Outline each Plasmodium ovale-infected red blood cell.
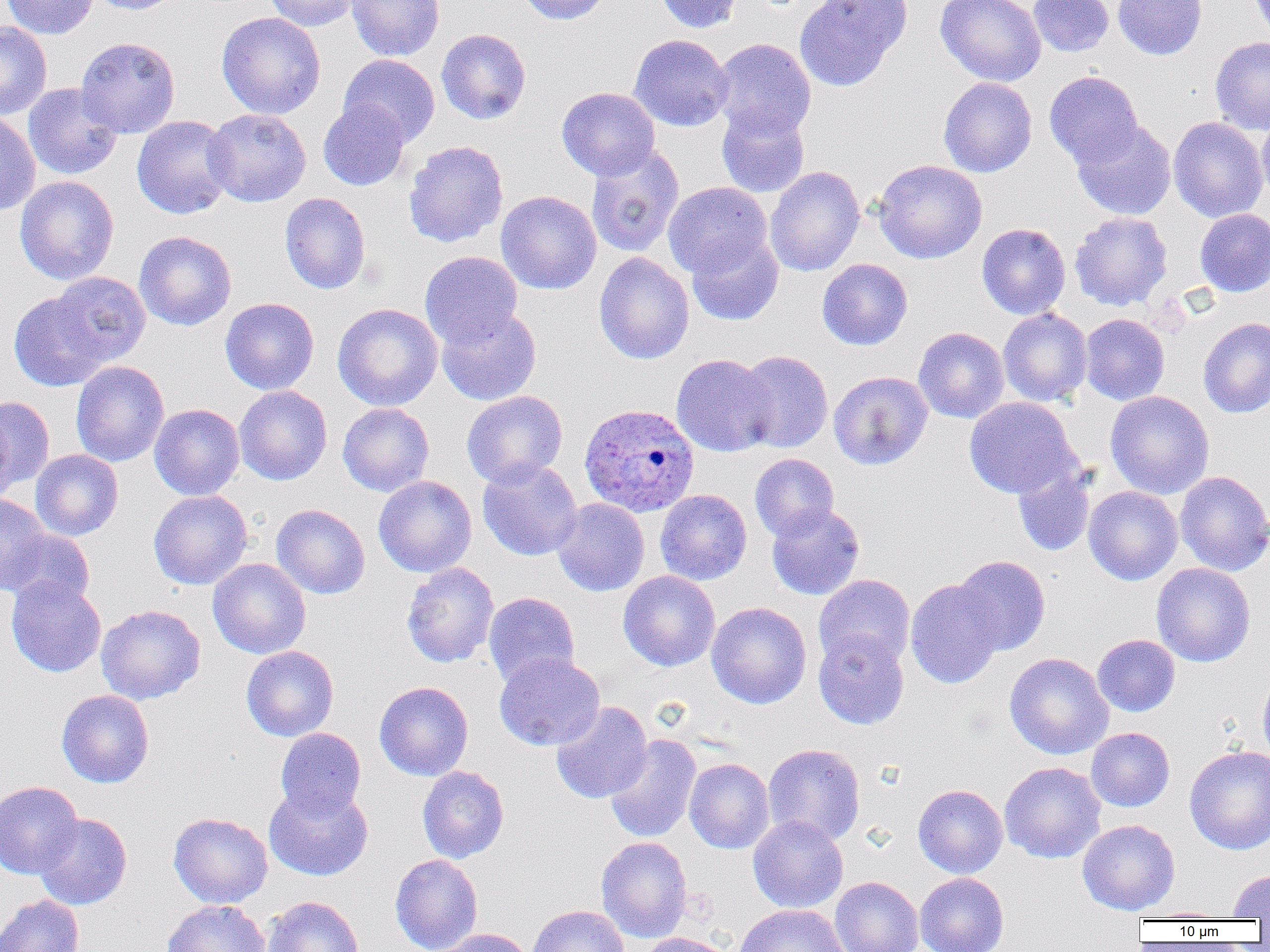
Approximate bounding boxes as (x1, y1, x2, y2) in pixels.
Plasmodium ovale-infected red blood cells: (579, 403, 699, 517).

Uninfected red blood cell locations: (2, 0, 98, 39), (86, 0, 184, 15), (262, 0, 360, 32), (346, 0, 445, 62), (517, 0, 611, 25), (653, 0, 743, 34), (794, 0, 912, 91), (934, 0, 1047, 87), (1028, 0, 1114, 57), (1113, 0, 1207, 60), (1249, 0, 1270, 39), (216, 12, 326, 119), (0, 21, 52, 119), (436, 28, 531, 125), (629, 34, 733, 132), (75, 36, 181, 138), (1210, 37, 1270, 134), (711, 38, 816, 140), (338, 54, 440, 147), (1044, 71, 1143, 168), (938, 77, 1037, 177), (23, 83, 123, 180), (556, 87, 660, 181), (318, 100, 410, 191), (716, 105, 810, 198), (203, 109, 311, 206), (0, 111, 40, 215), (1256, 111, 1270, 208), (131, 115, 236, 219), (1168, 117, 1268, 222), (1071, 120, 1177, 220), (403, 140, 508, 248), (585, 143, 684, 258), (873, 159, 987, 264), (765, 166, 865, 277), (14, 175, 119, 285), (663, 182, 772, 278), (496, 190, 601, 294), (280, 192, 371, 294), (1195, 208, 1270, 297), (1070, 211, 1172, 311), (977, 223, 1071, 320), (134, 231, 236, 331), (687, 233, 784, 326), (420, 250, 523, 347), (593, 252, 694, 364), (817, 259, 913, 350), (50, 271, 151, 366), (9, 291, 109, 391), (220, 297, 319, 395), (332, 303, 443, 411), (436, 305, 541, 405), (998, 308, 1093, 406), (1080, 313, 1170, 405), (1198, 318, 1270, 418), (913, 327, 1010, 424), (736, 350, 833, 453), (671, 354, 777, 457), (70, 360, 169, 467), (828, 370, 933, 470), (234, 385, 332, 485), (462, 390, 568, 488), (1105, 390, 1214, 499), (0, 395, 54, 495), (964, 397, 1079, 498), (0, 400, 19, 505), (337, 403, 435, 496), (149, 404, 244, 500), (30, 449, 123, 541), (749, 453, 839, 541), (477, 458, 583, 561), (1013, 464, 1096, 557), (1174, 470, 1270, 576), (373, 475, 477, 577), (1084, 486, 1183, 585), (148, 489, 252, 590), (655, 489, 752, 585), (0, 494, 51, 595), (552, 498, 650, 596), (766, 503, 865, 600), (271, 504, 370, 599), (2, 529, 94, 609), (951, 555, 1050, 656), (208, 558, 311, 659), (401, 561, 499, 668), (1151, 563, 1256, 667), (618, 571, 720, 671), (813, 574, 915, 670), (6, 576, 106, 677), (905, 578, 1006, 689), (483, 592, 580, 688), (706, 602, 811, 709), (96, 604, 205, 705), (813, 630, 909, 729), (1092, 634, 1180, 717), (241, 646, 339, 741), (494, 652, 605, 751), (1004, 653, 1114, 759), (1258, 671, 1270, 766), (374, 681, 473, 781), (56, 689, 154, 788), (551, 701, 652, 804), (1086, 727, 1175, 812), (275, 728, 366, 818), (604, 733, 701, 843), (763, 743, 866, 846), (1184, 744, 1270, 855), (684, 758, 775, 854), (999, 762, 1105, 863), (417, 766, 509, 863), (0, 781, 83, 878), (264, 783, 373, 881), (913, 784, 1008, 878), (168, 812, 273, 908), (34, 813, 132, 910), (748, 815, 848, 913), (1077, 819, 1180, 915), (595, 836, 693, 942), (390, 854, 483, 952), (1228, 868, 1270, 918), (915, 872, 1009, 952), (830, 876, 924, 952), (0, 895, 84, 952), (262, 896, 363, 952), (162, 899, 270, 952), (733, 904, 849, 952), (527, 905, 629, 952), (1138, 907, 1230, 921), (437, 928, 534, 952), (638, 932, 734, 952). Slide-level diagnosis: Plasmodium ovale. Single field of view. Captured at 1000x magnification. Optical microscopy. Thin blood film. Image is 1270×952 pixels.